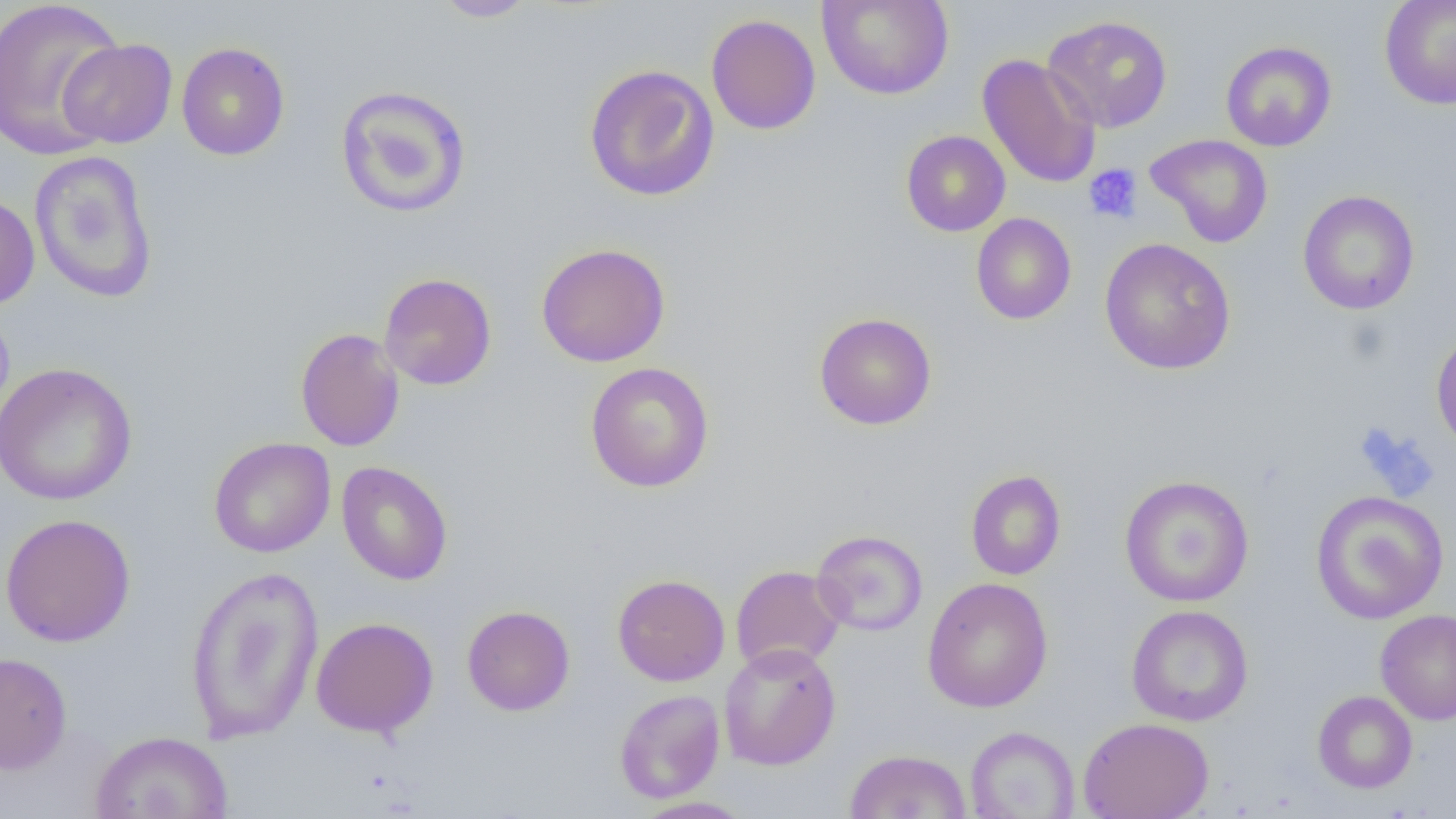 Approximate bounding boxes as (x1,y1)-(x2,y2) corner pairs in pixels. Platelet locations: (1083,163)-(1143,225). Uninfected red blood cell locations: (0,0)-(127,161), (434,0)-(538,22), (817,0)-(954,100), (1378,0)-(1456,110), (706,14)-(821,135), (1042,14)-(1174,133), (58,38)-(178,148), (1220,41)-(1337,151), (176,42)-(290,161), (977,53)-(1101,190), (583,64)-(720,202), (335,84)-(472,219), (901,130)-(1011,236), (1145,133)-(1273,248), (28,150)-(159,304), (1297,190)-(1420,315), (0,192)-(40,310), (971,212)-(1076,325), (1099,237)-(1236,375), (536,242)-(671,367), (379,273)-(497,391), (813,312)-(937,431), (295,328)-(405,452), (1431,328)-(1456,454), (585,361)-(714,493), (0,362)-(137,506), (208,437)-(335,558), (336,461)-(453,585), (965,469)-(1066,580), (1119,474)-(1254,607), (1310,490)-(1449,625), (0,513)-(136,647), (811,529)-(928,636), (184,565)-(324,744), (731,565)-(846,674), (612,573)-(730,686), (922,577)-(1053,713), (462,605)-(575,716), (1125,605)-(1253,726), (1375,609)-(1456,725), (311,616)-(439,737), (719,642)-(841,771), (0,651)-(72,774), (614,689)-(725,804), (1312,690)-(1417,793), (1077,717)-(1214,819), (965,726)-(1080,818), (91,731)-(234,818), (844,749)-(972,818), (632,796)-(755,818). Slide-level diagnosis: negative for blood parasites. Thin blood smear. Captured at 1000x magnification. Optical microscopy. Single field of view. Image is 1456×819 pixels.